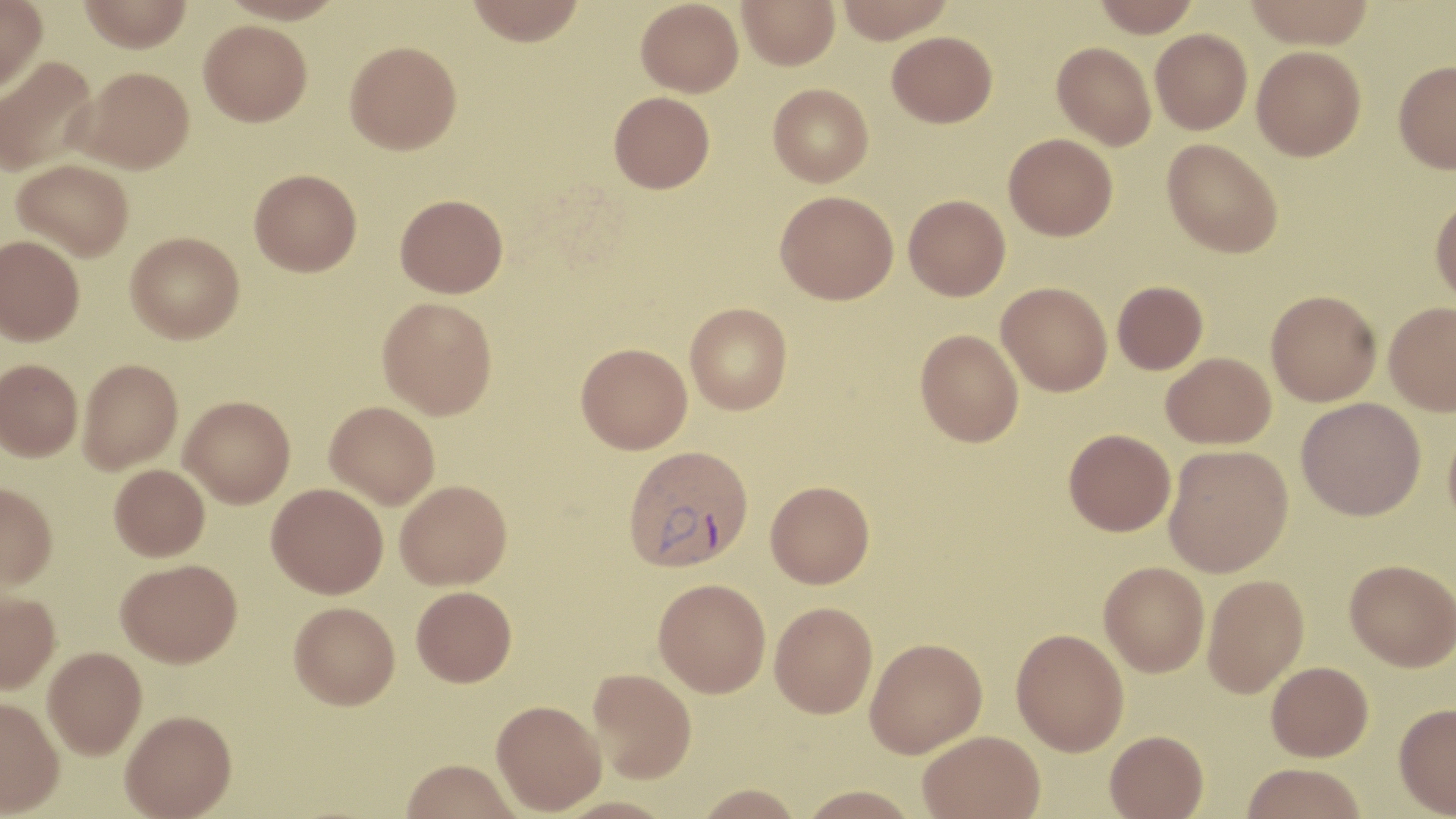

slide-level diagnosis = Plasmodium vivax
image size = 1456×819 pixels
uninfected red blood cell locations = approximate bounding boxes as named x1/y1/x2/y2 corners in pixels: (x1=0, y1=0, x2=47, y2=93), (x1=79, y1=0, x2=192, y2=52), (x1=218, y1=0, x2=347, y2=25), (x1=466, y1=0, x2=586, y2=45), (x1=636, y1=0, x2=743, y2=97), (x1=737, y1=0, x2=840, y2=69), (x1=834, y1=0, x2=955, y2=43), (x1=1092, y1=0, x2=1201, y2=37), (x1=1244, y1=0, x2=1375, y2=49), (x1=199, y1=19, x2=312, y2=126), (x1=1150, y1=29, x2=1252, y2=134), (x1=887, y1=30, x2=997, y2=127), (x1=344, y1=40, x2=461, y2=154), (x1=1052, y1=42, x2=1157, y2=150), (x1=1252, y1=45, x2=1366, y2=161), (x1=0, y1=55, x2=99, y2=177), (x1=1394, y1=60, x2=1456, y2=173), (x1=74, y1=66, x2=195, y2=173), (x1=768, y1=83, x2=873, y2=187), (x1=608, y1=91, x2=715, y2=193), (x1=1004, y1=133, x2=1118, y2=240), (x1=1162, y1=138, x2=1283, y2=257), (x1=12, y1=158, x2=134, y2=261), (x1=249, y1=168, x2=361, y2=276), (x1=775, y1=190, x2=899, y2=304), (x1=395, y1=193, x2=508, y2=297), (x1=904, y1=194, x2=1010, y2=300), (x1=1430, y1=196, x2=1456, y2=306), (x1=126, y1=231, x2=244, y2=343), (x1=0, y1=234, x2=84, y2=345), (x1=1112, y1=281, x2=1208, y2=374), (x1=996, y1=282, x2=1112, y2=396), (x1=1266, y1=289, x2=1381, y2=406), (x1=377, y1=296, x2=497, y2=419), (x1=685, y1=302, x2=793, y2=414), (x1=1384, y1=302, x2=1456, y2=415), (x1=915, y1=329, x2=1024, y2=447), (x1=576, y1=342, x2=692, y2=453), (x1=1161, y1=352, x2=1276, y2=448), (x1=78, y1=358, x2=183, y2=474), (x1=0, y1=359, x2=83, y2=461), (x1=180, y1=395, x2=295, y2=507), (x1=1296, y1=397, x2=1425, y2=520), (x1=324, y1=401, x2=440, y2=509), (x1=1444, y1=416, x2=1456, y2=536), (x1=1064, y1=429, x2=1175, y2=536), (x1=1164, y1=444, x2=1294, y2=577), (x1=109, y1=464, x2=209, y2=561), (x1=395, y1=479, x2=512, y2=589), (x1=765, y1=480, x2=874, y2=588), (x1=0, y1=482, x2=58, y2=590), (x1=266, y1=483, x2=388, y2=598), (x1=116, y1=558, x2=242, y2=666), (x1=1345, y1=559, x2=1456, y2=671), (x1=1099, y1=562, x2=1209, y2=677), (x1=1202, y1=574, x2=1309, y2=697), (x1=653, y1=578, x2=771, y2=697), (x1=411, y1=586, x2=517, y2=686), (x1=0, y1=590, x2=60, y2=694), (x1=289, y1=601, x2=400, y2=709), (x1=770, y1=602, x2=877, y2=718), (x1=1011, y1=628, x2=1129, y2=755), (x1=864, y1=638, x2=987, y2=757), (x1=43, y1=646, x2=146, y2=759), (x1=1266, y1=661, x2=1373, y2=761), (x1=587, y1=668, x2=697, y2=782), (x1=0, y1=697, x2=63, y2=817), (x1=491, y1=699, x2=606, y2=815), (x1=1394, y1=702, x2=1456, y2=816), (x1=120, y1=710, x2=237, y2=819), (x1=917, y1=729, x2=1044, y2=819), (x1=1105, y1=729, x2=1209, y2=818), (x1=400, y1=759, x2=521, y2=819), (x1=1240, y1=762, x2=1368, y2=819), (x1=693, y1=784, x2=804, y2=819), (x1=797, y1=785, x2=920, y2=818)
field of view = single
magnification = 1000x
preparation = thin blood film
Plasmodium vivax-infected red blood cell locations = approximate bounding boxes as named x1/y1/x2/y2 corners in pixels: (x1=622, y1=444, x2=754, y2=573)
stain = May-Grünwald-Giemsa
modality = optical microscopy